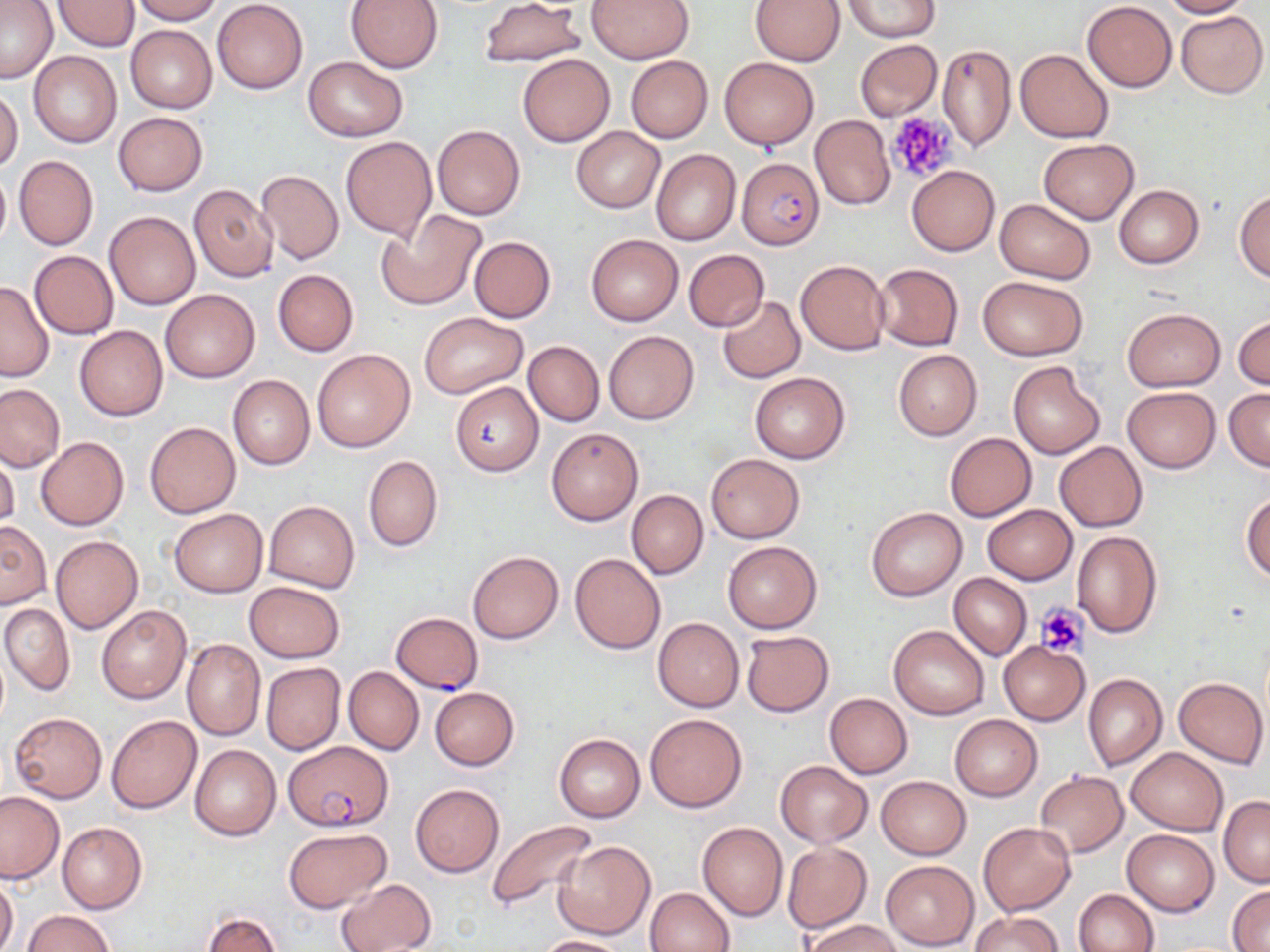
Summary:
  - Coordinate format: approximate bounding boxes as (x1,y1)-(x2,y2) corner pairs in pixels
  - Platelet locations: (887,112)-(958,183), (1036,603)-(1088,658)
  - Plasmodium falciparum-infected red blood cell locations: (737,156)-(824,250), (390,612)-(484,693), (284,740)-(395,831)
  - Uninfected red blood cell locations: (1,0)-(58,84), (129,0)-(222,24), (347,0)-(444,71), (478,0)-(586,67), (586,0)-(695,64), (843,0)-(938,41), (1160,0)-(1248,18), (212,1)-(307,94), (751,1)-(844,66), (1082,1)-(1177,92), (53,2)-(139,52), (1175,11)-(1268,98), (125,24)-(217,113), (854,39)-(942,122), (937,44)-(1016,152), (1015,49)-(1113,142), (28,50)-(121,148), (517,52)-(615,147), (626,55)-(712,143), (301,56)-(409,142), (719,56)-(818,150), (0,87)-(23,173), (113,112)-(208,196), (809,115)-(895,210), (433,124)-(525,219), (572,126)-(665,213), (340,136)-(436,240), (1039,139)-(1138,224), (651,148)-(741,246), (14,155)-(98,250), (0,166)-(11,252), (907,166)-(999,256), (256,169)-(344,264), (189,184)-(278,282), (1114,184)-(1204,268), (1234,190)-(1270,280), (995,199)-(1094,285), (104,209)-(202,310), (377,210)-(487,310), (587,235)-(682,326), (468,236)-(556,323), (29,250)-(118,338), (684,250)-(770,330), (795,259)-(890,355), (873,263)-(963,351), (272,269)-(359,357), (977,276)-(1087,360), (0,280)-(54,381), (160,289)-(259,383), (718,296)-(805,383), (1122,308)-(1226,390), (419,311)-(526,398), (1234,316)-(1270,390), (74,325)-(169,421), (603,330)-(699,424), (523,341)-(604,426), (312,348)-(416,453), (893,350)-(982,440), (1007,361)-(1105,459), (749,371)-(850,464), (228,375)-(315,470), (450,381)-(543,476), (0,384)-(64,472), (1121,387)-(1221,473), (1224,388)-(1270,471), (145,422)-(241,518), (545,427)-(643,527), (944,432)-(1036,521), (36,436)-(129,530), (1054,441)-(1146,532), (0,448)-(20,532), (706,454)-(804,542), (363,455)-(443,553), (626,490)-(708,579), (1242,492)-(1270,581), (264,500)-(360,592), (981,504)-(1076,584), (867,506)-(967,601), (169,508)-(268,597), (0,521)-(51,609), (1071,530)-(1162,637), (51,536)-(142,632), (722,541)-(822,634), (467,550)-(564,643), (570,553)-(665,653), (949,573)-(1031,660), (243,581)-(345,663), (1,602)-(75,695), (97,604)-(191,704), (653,618)-(744,711), (889,624)-(989,720), (741,631)-(835,716), (182,638)-(266,740), (998,640)-(1091,725), (261,662)-(345,756), (344,666)-(423,755), (1083,673)-(1167,770), (1173,677)-(1267,768), (430,686)-(520,770), (825,693)-(912,778), (8,712)-(107,803), (645,713)-(748,813), (949,714)-(1041,801), (106,716)-(202,814), (554,733)-(645,822), (189,744)-(281,840), (1127,747)-(1227,835), (774,760)-(872,847), (1036,771)-(1127,857), (876,777)-(971,859), (411,784)-(503,877), (0,791)-(65,884), (1219,797)-(1270,887), (487,818)-(597,912), (57,822)-(147,914), (697,822)-(787,921), (977,822)-(1075,916), (283,827)-(391,911), (1122,829)-(1219,915), (555,841)-(655,940), (783,843)-(870,933), (880,860)-(979,949), (337,877)-(437,952), (0,878)-(18,952), (1228,884)-(1270,949), (644,888)-(733,952), (1073,889)-(1158,952), (971,910)-(1061,952), (23,911)-(113,952), (202,911)-(282,951), (804,917)-(903,952), (536,935)-(627,952)
  - Slide-level diagnosis: Plasmodium falciparum
  - Image size: 1270×952 pixels
  - Field of view: single
  - Modality: optical microscopy
  - Preparation: thin blood smear
  - Magnification: 1000x
  - Stain: May-Grünwald-Giemsa